State which parasite is depicted.
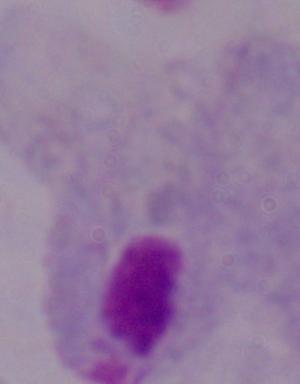
A trichomonad.

magnification = 1000x
modality = micrograph